Report the malaria status of this cell.
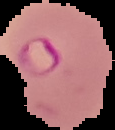
Parasitized.

image size = 115×130 pixels
preparation = thin blood smear
image type = segmented cell region on a black background